Classify this cell by malaria status.
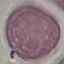

Uninfected.

capture = smartphone through the microscope eyepiece
image type = automatically extracted cell patch, resized to 64 × 64 pixels
preparation = thin smear
stain = Giemsa